State which parasite is depicted.
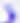

This is Toxoplasma gondii.

Summary:
  - Modality: photomicrograph
  - Magnification: 400x